Assess this cell for malaria.
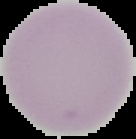
It is uninfected.

image size = 136×139 pixels
preparation = thin blood smear
image type = cell region segmented out of the field of view; surrounding area masked to black